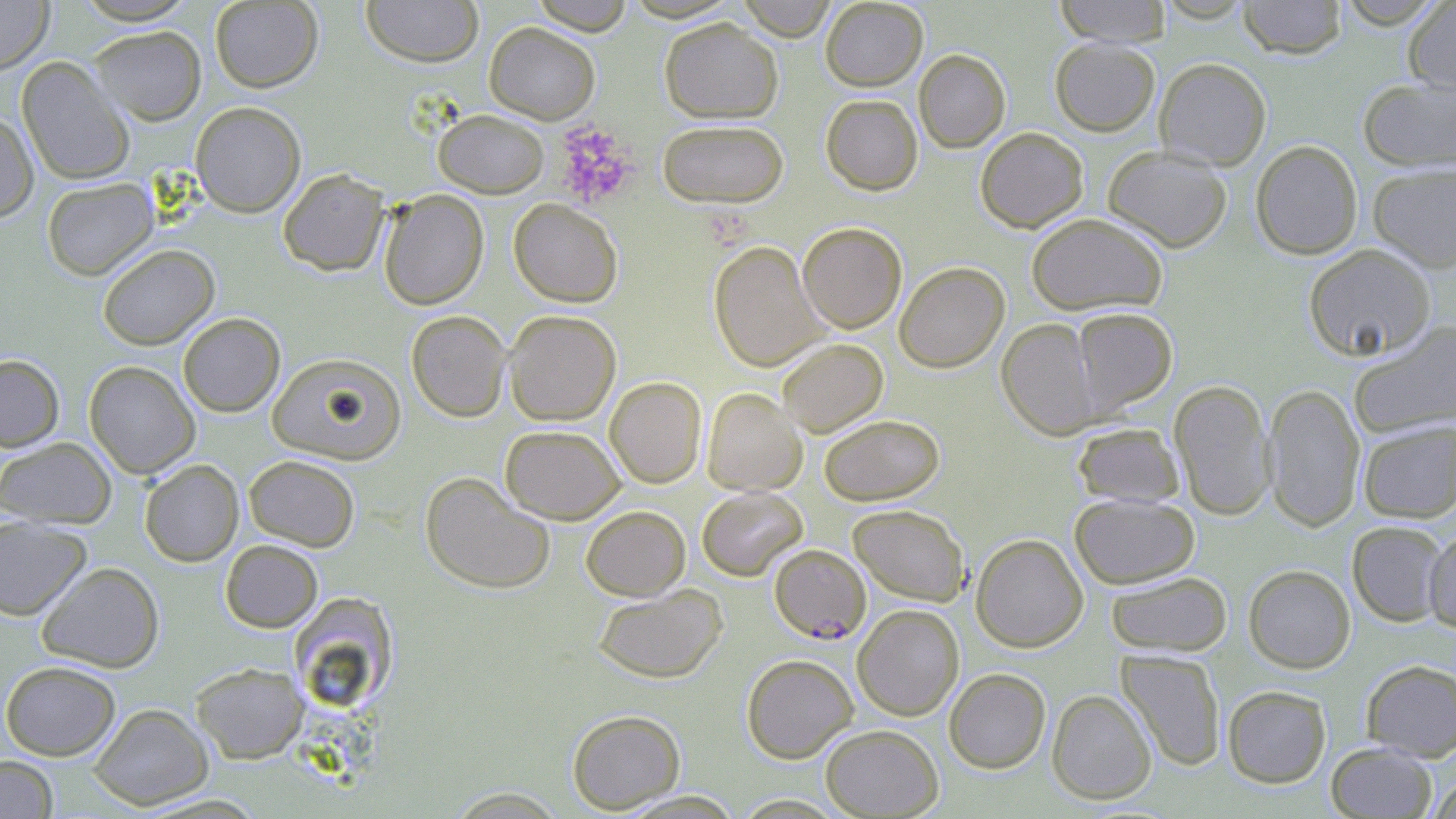
slide-level diagnosis = Plasmodium falciparum
preparation = thin blood smear
platelet locations = approximate bounding boxes as named x1/y1/x2/y2 corners in pixels: (x1=553, y1=121, x2=639, y2=208)
magnification = 1000x
Plasmodium falciparum-infected red blood cell locations = approximate bounding boxes as named x1/y1/x2/y2 corners in pixels: (x1=769, y1=544, x2=871, y2=644)
stain = May-Grünwald-Giemsa
modality = light microscopy
uninfected red blood cell locations = approximate bounding boxes as named x1/y1/x2/y2 corners in pixels: (x1=0, y1=0, x2=54, y2=74), (x1=72, y1=0, x2=199, y2=24), (x1=361, y1=0, x2=484, y2=67), (x1=529, y1=0, x2=636, y2=35), (x1=736, y1=0, x2=837, y2=40), (x1=820, y1=0, x2=929, y2=91), (x1=1054, y1=0, x2=1172, y2=46), (x1=1238, y1=0, x2=1347, y2=59), (x1=1335, y1=0, x2=1447, y2=28), (x1=209, y1=1, x2=323, y2=92), (x1=1403, y1=1, x2=1456, y2=96), (x1=659, y1=18, x2=783, y2=123), (x1=484, y1=22, x2=600, y2=124), (x1=89, y1=26, x2=206, y2=125), (x1=1050, y1=37, x2=1160, y2=136), (x1=914, y1=49, x2=1010, y2=152), (x1=17, y1=56, x2=134, y2=186), (x1=1154, y1=57, x2=1272, y2=170), (x1=1358, y1=76, x2=1456, y2=172), (x1=821, y1=94, x2=922, y2=195), (x1=191, y1=101, x2=306, y2=217), (x1=433, y1=109, x2=549, y2=198), (x1=0, y1=111, x2=39, y2=222), (x1=657, y1=119, x2=789, y2=207), (x1=975, y1=127, x2=1088, y2=232), (x1=1251, y1=140, x2=1362, y2=259), (x1=1102, y1=145, x2=1233, y2=253), (x1=1367, y1=163, x2=1456, y2=272), (x1=278, y1=168, x2=389, y2=276), (x1=41, y1=178, x2=159, y2=281), (x1=379, y1=190, x2=489, y2=310), (x1=509, y1=198, x2=623, y2=307), (x1=1026, y1=212, x2=1168, y2=316), (x1=798, y1=222, x2=907, y2=333), (x1=708, y1=241, x2=828, y2=372), (x1=98, y1=244, x2=219, y2=350), (x1=1303, y1=244, x2=1436, y2=362), (x1=894, y1=261, x2=1009, y2=373), (x1=1072, y1=307, x2=1177, y2=412), (x1=406, y1=310, x2=511, y2=422), (x1=503, y1=310, x2=621, y2=426), (x1=178, y1=313, x2=285, y2=417), (x1=997, y1=318, x2=1102, y2=439), (x1=1350, y1=321, x2=1456, y2=439), (x1=777, y1=338, x2=888, y2=437), (x1=267, y1=352, x2=405, y2=465), (x1=0, y1=354, x2=64, y2=451), (x1=84, y1=360, x2=200, y2=478), (x1=605, y1=377, x2=707, y2=488), (x1=1169, y1=379, x2=1275, y2=520), (x1=1263, y1=383, x2=1366, y2=532), (x1=702, y1=387, x2=806, y2=496), (x1=818, y1=414, x2=945, y2=506), (x1=1357, y1=419, x2=1456, y2=522), (x1=1072, y1=422, x2=1185, y2=508), (x1=500, y1=425, x2=625, y2=524), (x1=0, y1=437, x2=117, y2=529), (x1=244, y1=455, x2=360, y2=551), (x1=139, y1=459, x2=244, y2=566), (x1=420, y1=471, x2=555, y2=594), (x1=696, y1=487, x2=807, y2=581), (x1=1069, y1=493, x2=1199, y2=589), (x1=848, y1=504, x2=969, y2=605), (x1=580, y1=505, x2=691, y2=600), (x1=0, y1=516, x2=92, y2=620), (x1=1347, y1=521, x2=1448, y2=626), (x1=1424, y1=525, x2=1456, y2=634), (x1=971, y1=533, x2=1088, y2=652), (x1=220, y1=539, x2=322, y2=632), (x1=36, y1=561, x2=164, y2=672), (x1=1243, y1=564, x2=1355, y2=673), (x1=1106, y1=571, x2=1232, y2=656), (x1=593, y1=585, x2=727, y2=683), (x1=287, y1=593, x2=399, y2=714), (x1=852, y1=604, x2=964, y2=720), (x1=1116, y1=650, x2=1226, y2=770), (x1=741, y1=654, x2=858, y2=763), (x1=1360, y1=659, x2=1456, y2=761), (x1=1, y1=660, x2=121, y2=760), (x1=191, y1=662, x2=308, y2=763), (x1=944, y1=668, x2=1051, y2=773), (x1=1222, y1=685, x2=1331, y2=788), (x1=1047, y1=689, x2=1157, y2=804), (x1=88, y1=703, x2=213, y2=810), (x1=567, y1=709, x2=685, y2=813), (x1=820, y1=724, x2=943, y2=818), (x1=1326, y1=742, x2=1436, y2=818), (x1=0, y1=756, x2=58, y2=818), (x1=1427, y1=774, x2=1456, y2=818), (x1=446, y1=787, x2=568, y2=817), (x1=615, y1=790, x2=745, y2=818)
field of view = single
image size = 1456×819 pixels